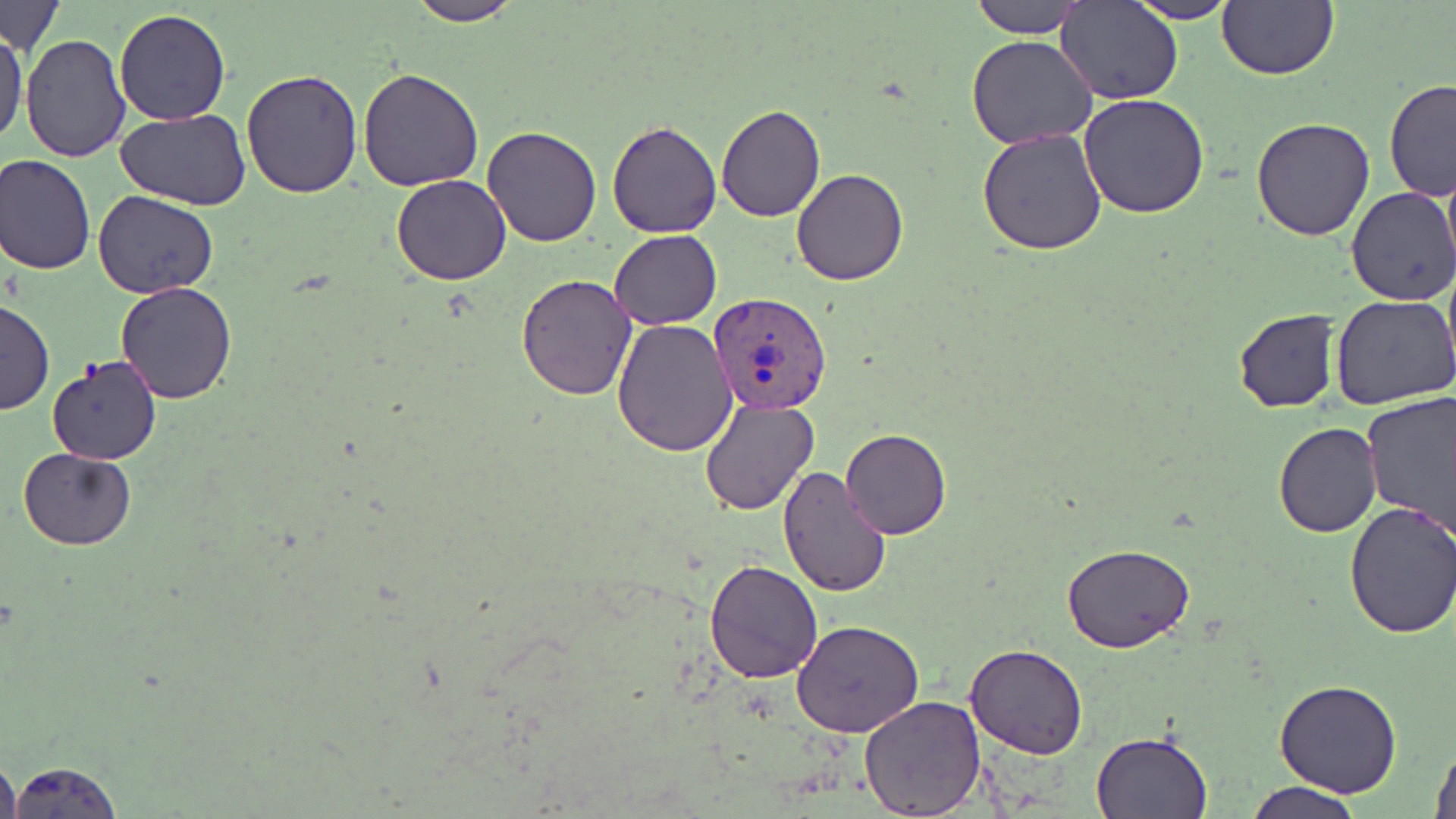
slide-level diagnosis = Plasmodium vivax
field of view = single
uninfected red blood cell locations = approximate bounding boxes as (x1, y1, x2, y2) in pixels: (969, 0, 1088, 39), (1056, 0, 1183, 104), (1218, 0, 1339, 80), (403, 1, 526, 25), (1127, 1, 1241, 24), (2, 2, 66, 55), (114, 9, 231, 125), (0, 30, 27, 147), (20, 34, 131, 162), (966, 34, 1098, 148), (358, 66, 486, 191), (241, 67, 363, 197), (1383, 80, 1456, 203), (1078, 94, 1210, 218), (716, 104, 824, 221), (118, 107, 251, 210), (1251, 116, 1376, 240), (606, 120, 722, 238), (482, 125, 602, 247), (977, 128, 1107, 254), (1440, 151, 1456, 287), (1, 154, 96, 276), (791, 168, 908, 285), (391, 175, 512, 286), (1346, 186, 1456, 306), (93, 190, 218, 297), (608, 229, 721, 329), (516, 274, 636, 400), (115, 282, 237, 404), (1332, 292, 1456, 410), (0, 298, 55, 415), (1234, 309, 1341, 414), (613, 316, 740, 456), (45, 357, 161, 465), (1361, 391, 1456, 536), (700, 397, 818, 515), (1274, 423, 1382, 538), (840, 428, 950, 540), (19, 447, 135, 548), (775, 464, 891, 597), (1345, 501, 1456, 639), (1062, 542, 1197, 654), (703, 559, 823, 683), (793, 620, 924, 737), (966, 642, 1087, 757), (1275, 680, 1402, 798), (858, 695, 986, 816), (1091, 730, 1212, 818), (1429, 740, 1456, 819), (0, 753, 23, 818), (6, 761, 125, 817), (1245, 780, 1364, 819)
image size = 1456×819 pixels
modality = optical microscopy
preparation = thin blood film
Plasmodium vivax-infected red blood cell locations = approximate bounding boxes as (x1, y1, x2, y2) in pixels: (709, 291, 832, 414)
magnification = 1000x
stain = May-Grünwald-Giemsa